Comment on the morphology of the red blood cells.
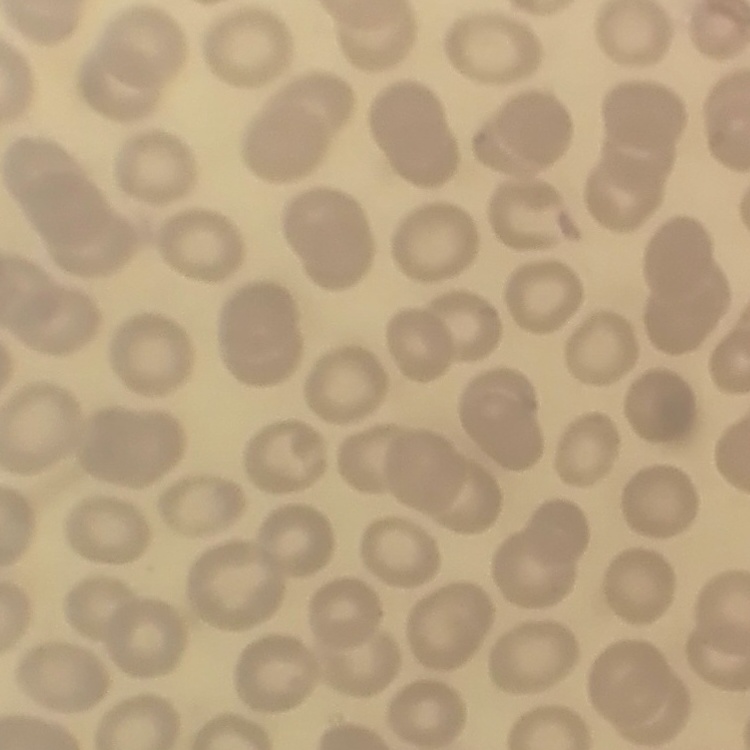
They show no rouleaux formation.

image type = square crop of a larger photomicrograph
preparation = thin peripheral smear
stain = Field's or Giemsa